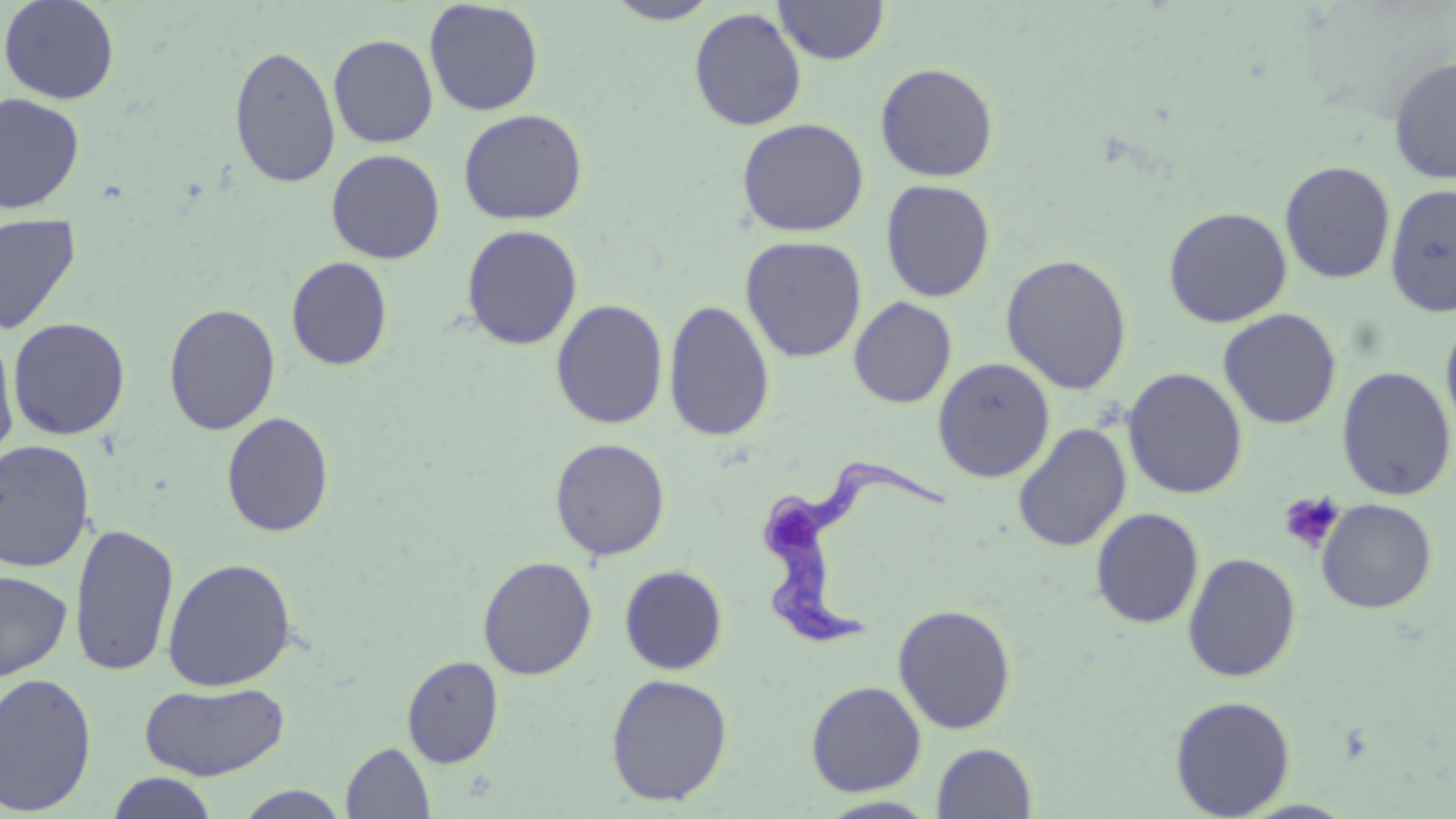
Summary:
  - Coordinate format: approximate bounding boxes as (x1,y1)-(x2,y2) corner pairs in pixels
  - Uninfected red blood cell locations: (1,0)-(120,104), (424,1)-(545,116), (604,1)-(720,25), (774,1)-(889,65), (689,7)-(807,131), (328,33)-(438,148), (228,45)-(341,188), (1388,55)-(1456,184), (875,62)-(999,182), (0,92)-(84,214), (458,108)-(588,225), (736,117)-(870,237), (326,149)-(446,264), (1279,160)-(1396,284), (880,179)-(996,302), (1384,182)-(1456,317), (1163,206)-(1292,327), (0,212)-(81,335), (461,224)-(583,350), (740,235)-(867,363), (1000,252)-(1133,395), (286,257)-(393,371), (849,296)-(958,408), (550,299)-(669,430), (663,299)-(776,442), (163,303)-(281,436), (1218,308)-(1342,429), (1440,310)-(1456,445), (4,315)-(108,568), (7,317)-(131,440), (0,326)-(19,464), (931,357)-(1055,483), (1336,366)-(1455,501), (1122,367)-(1248,500), (221,412)-(335,538), (1012,423)-(1131,552), (550,437)-(671,561), (0,440)-(96,573), (1316,499)-(1437,614), (1090,508)-(1204,629), (69,523)-(179,678), (1182,552)-(1302,682), (478,556)-(598,680), (162,557)-(297,691), (619,564)-(728,675), (0,570)-(73,680), (892,603)-(1017,734), (402,655)-(503,767), (0,671)-(98,815), (605,673)-(733,806), (139,680)-(290,781), (806,680)-(927,796), (1169,695)-(1296,818), (341,742)-(436,818), (932,742)-(1038,819), (105,772)-(220,819), (817,796)-(941,818)
  - Trypanosoma brucei locations: (760,458)-(948,650)
  - Platelet locations: (1278,490)-(1346,555)
  - Slide-level diagnosis: Trypanosoma brucei
  - Field of view: one of a larger specimen
  - Modality: optical microscopy
  - Stain: May-Grünwald-Giemsa
  - Image size: 1456×819 pixels
  - Preparation: thin blood film
  - Magnification: 1000x